Comment on the morphology of the red blood cells.
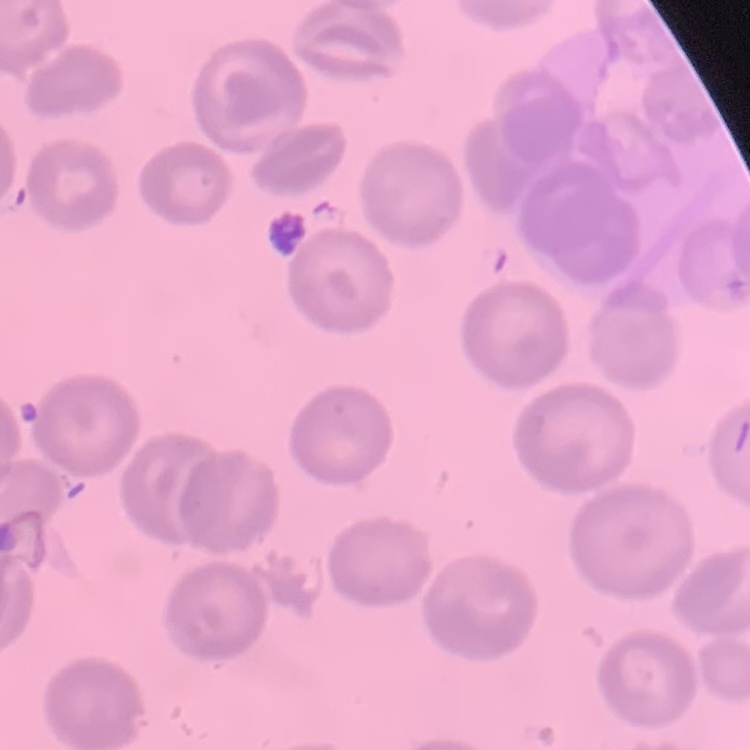

No rouleaux formation.

image type = one tile cut from a larger photomicrograph
stain = Field's or Giemsa
preparation = thin blood smear